Report the malaria status of this cell.
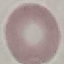
It is uninfected.

Photographed with a smartphone camera at the microscope eyepiece. Giemsa stain. Thin blood smear. Cell patch, automatically extracted from a larger field of view and resized to 64 × 64 pixels.